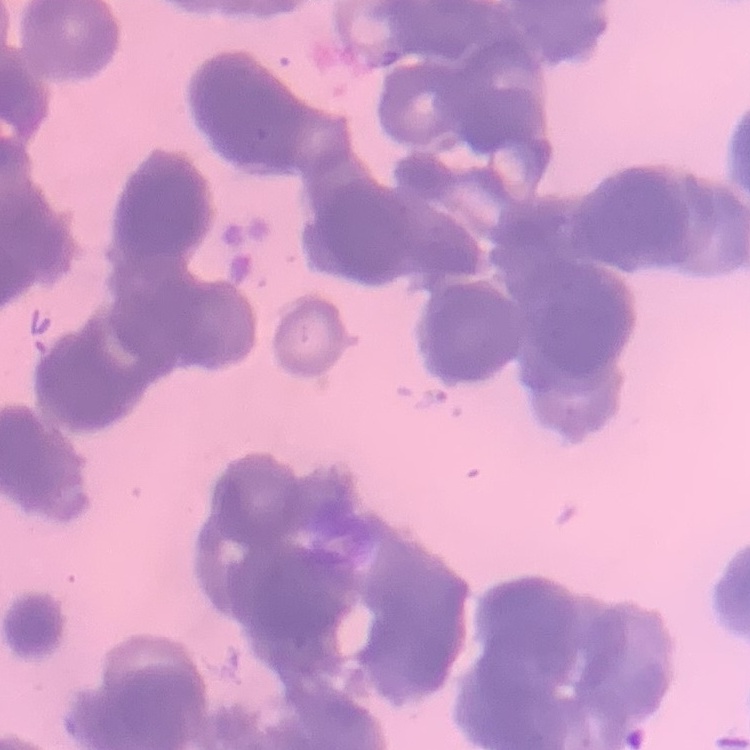

Summary:
  - Red blood cell morphology: rouleaux formation
  - Stain: Field's or Giemsa
  - Preparation: thin blood smear
  - Image type: one tile cut from a larger photomicrograph